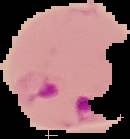
image type = cell region segmented out of the field of view; surrounding area masked to black
malaria status = parasitized
preparation = thin blood smear
image size = 130×139 pixels